Describe the morphology of the red blood cells.
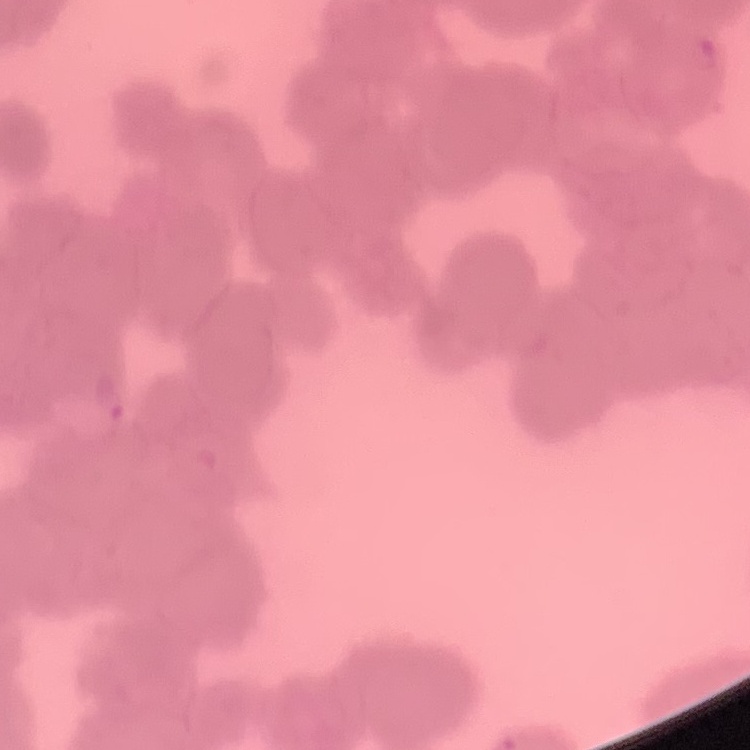
Rouleaux formation.

Thin blood smear. Field's or Giemsa stain. Square crop of a larger photomicrograph.